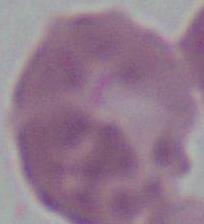
Summary:
  - Identification: red blood cell
  - Magnification: 1000x
  - Modality: photomicrograph